Report the malaria status of this cell.
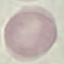
Uninfected.

image type = cell patch, automatically extracted from a larger field of view and resized to 64 × 64 pixels
capture = smartphone camera at the microscope eyepiece
stain = Giemsa
preparation = thin blood film